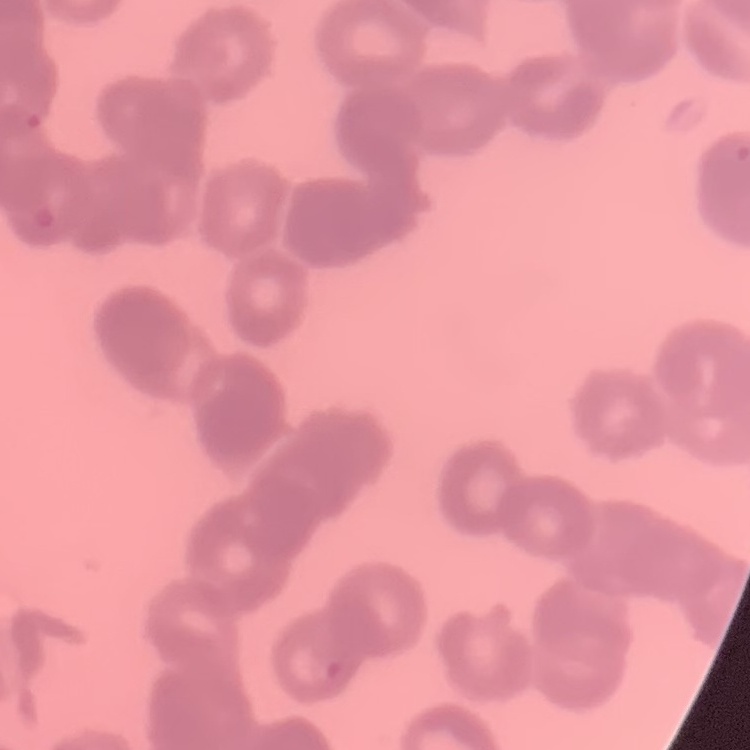
{
  "red_blood_cell_morphology": "rouleaux formation",
  "preparation": "thin peripheral smear",
  "stain": "Field's or Giemsa",
  "image_type": "one tile cut from a larger photomicrograph"
}